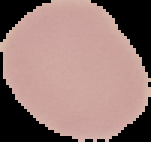

image size = 151×142 pixels
result = no Plasmodium parasites seen
image type = cell region segmented out of the field of view; surrounding area masked to black
preparation = thin blood film